Classify this cell by malaria status.
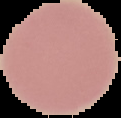

It is uninfected.

Image is 121×118 pixels. From a thin blood smear. Cell region segmented out of the field of view; the surrounding area is masked to black.